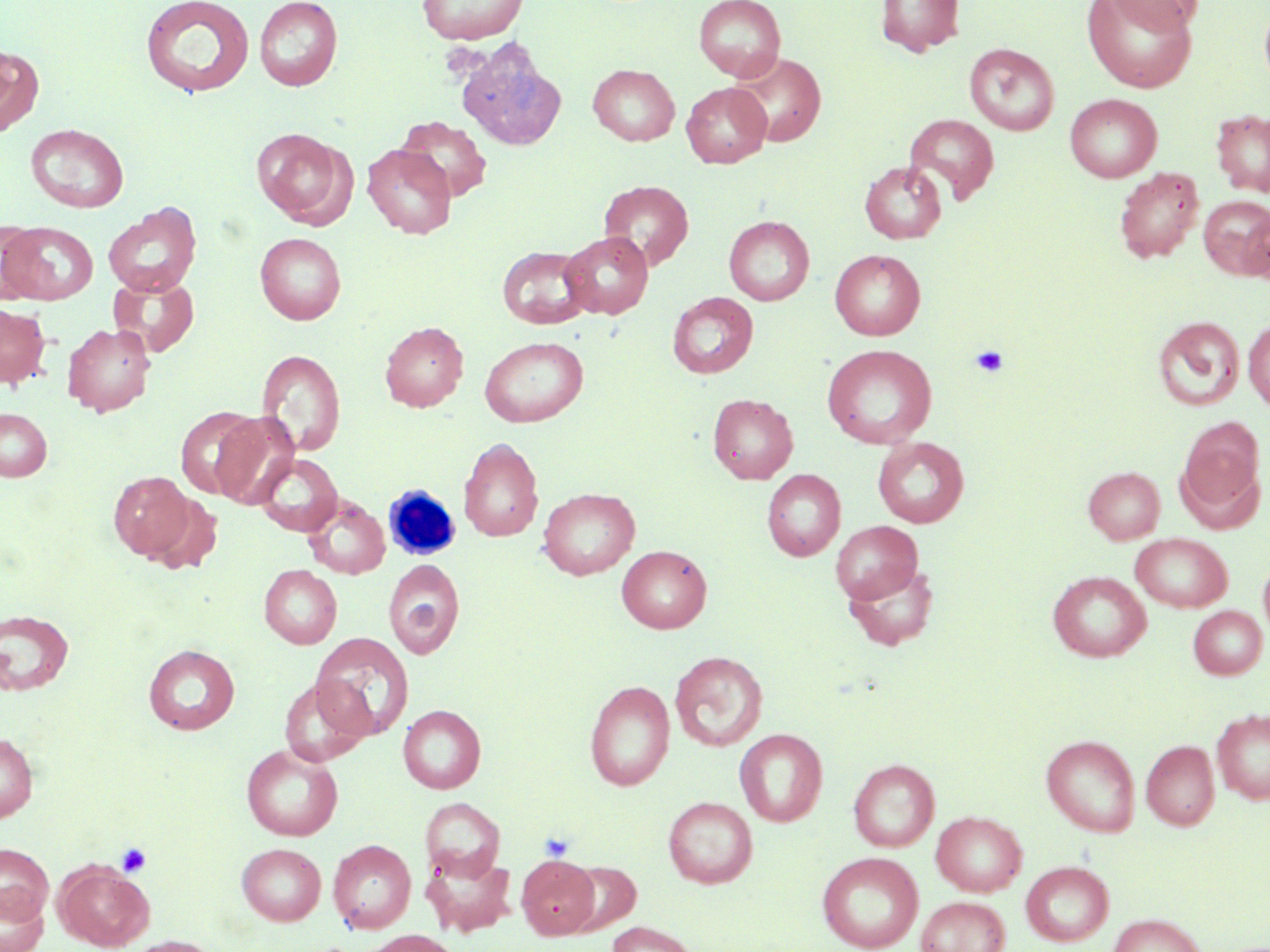

Summary:
  - Coordinate format: approximate bounding boxes as [x1, y1, x2, y2] in pixels
  - Uninfected red blood cell locations: [416, 0, 529, 44], [693, 0, 786, 82], [876, 0, 965, 57], [1084, 0, 1196, 91], [1105, 0, 1205, 34], [140, 1, 255, 99], [254, 1, 343, 90], [1259, 2, 1270, 94], [456, 42, 568, 151], [964, 43, 1060, 135], [0, 45, 43, 137], [731, 51, 827, 148], [588, 64, 680, 146], [681, 82, 771, 168], [1065, 93, 1162, 182], [1211, 108, 1270, 197], [903, 113, 999, 205], [396, 116, 492, 202], [26, 124, 128, 213], [252, 128, 353, 227], [362, 143, 456, 239], [860, 161, 947, 244], [1114, 167, 1204, 263], [598, 180, 693, 270], [1198, 196, 1270, 279], [103, 202, 202, 298], [1236, 203, 1270, 283], [724, 215, 815, 305], [0, 220, 44, 302], [1, 222, 98, 304], [560, 231, 654, 319], [255, 232, 346, 324], [497, 245, 593, 329], [830, 249, 925, 340], [108, 274, 199, 357], [667, 292, 758, 379], [0, 303, 50, 388], [1152, 316, 1245, 411], [1243, 318, 1270, 412], [380, 321, 468, 412], [62, 323, 156, 416], [479, 336, 588, 427], [822, 344, 937, 448], [257, 349, 345, 456], [707, 394, 798, 484], [174, 406, 261, 499], [0, 407, 52, 482], [211, 411, 299, 509], [1178, 417, 1265, 515], [873, 436, 969, 527], [458, 437, 543, 542], [254, 453, 343, 536], [1083, 466, 1165, 544], [761, 469, 846, 561], [108, 471, 195, 560], [538, 487, 640, 580], [145, 493, 224, 574], [304, 495, 390, 578], [831, 521, 923, 603], [1130, 533, 1233, 612], [617, 545, 712, 633], [1258, 556, 1270, 644], [384, 559, 465, 659], [842, 561, 940, 651], [259, 565, 342, 649], [1047, 571, 1152, 662], [1188, 605, 1267, 679], [0, 609, 74, 695], [310, 633, 414, 739], [143, 644, 240, 735], [669, 651, 768, 751], [279, 676, 373, 766], [584, 680, 675, 790], [398, 705, 486, 793], [1212, 707, 1270, 804], [734, 728, 828, 827], [0, 732, 38, 822], [1041, 735, 1140, 837], [1141, 740, 1220, 830], [242, 744, 343, 841], [848, 759, 939, 852], [663, 796, 757, 888], [421, 798, 505, 880], [931, 811, 1027, 896], [328, 839, 416, 933], [0, 842, 54, 923], [236, 843, 327, 925], [421, 849, 517, 937], [817, 851, 924, 952], [517, 854, 600, 940], [1020, 860, 1114, 947], [54, 861, 154, 950], [563, 861, 641, 935], [0, 887, 49, 952], [916, 896, 1010, 952], [1107, 913, 1208, 952], [606, 921, 700, 952], [362, 930, 460, 952], [121, 936, 224, 952]
  - Platelet locations: [971, 345, 1010, 377], [539, 831, 574, 862], [116, 842, 152, 877]
  - White blood cell locations: [383, 486, 460, 561]
  - Slide-level diagnosis: no evidence of blood parasites
  - Preparation: thin blood smear
  - Field of view: one of a larger specimen
  - Stain: May-Grünwald-Giemsa
  - Modality: optical microscopy
  - Image size: 1270×952 pixels
  - Magnification: 1000x